Classify this cell by malaria status.
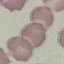
Uninfected.

image type = automatically extracted cell patch, resized to 64 × 64 pixels
capture = smartphone through the microscope eyepiece
stain = Giemsa
preparation = thin blood film